Describe the morphology of the erythrocytes.
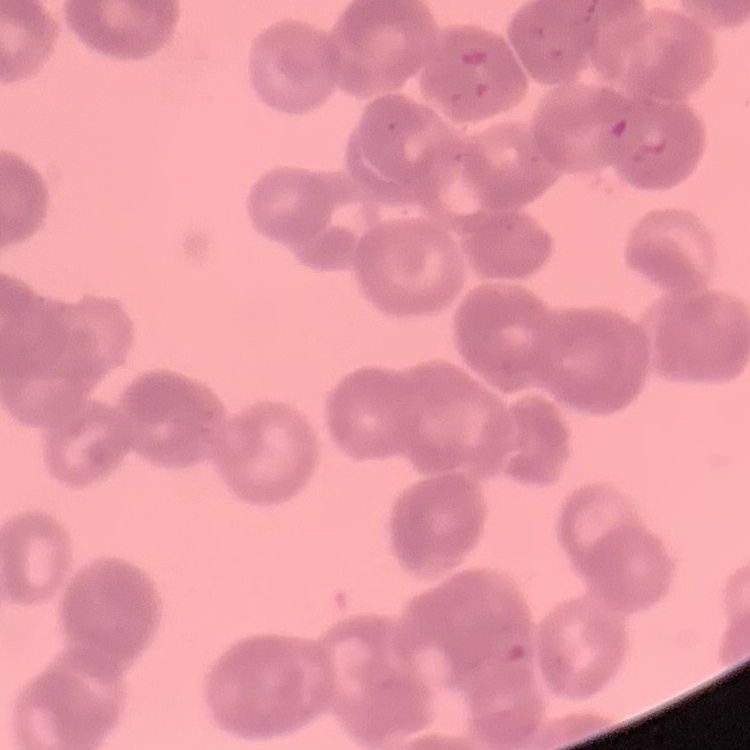

They show rouleaux formation.

preparation = thin blood smear
image type = square crop of a larger photomicrograph
stain = Field's or Giemsa